Assess this cell for malaria.
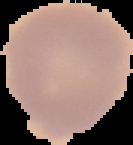

It is uninfected.

Summary:
  - Preparation: thin blood film
  - Image type: cell region segmented out of the field of view; surrounding area masked to black
  - Image size: 133×145 pixels